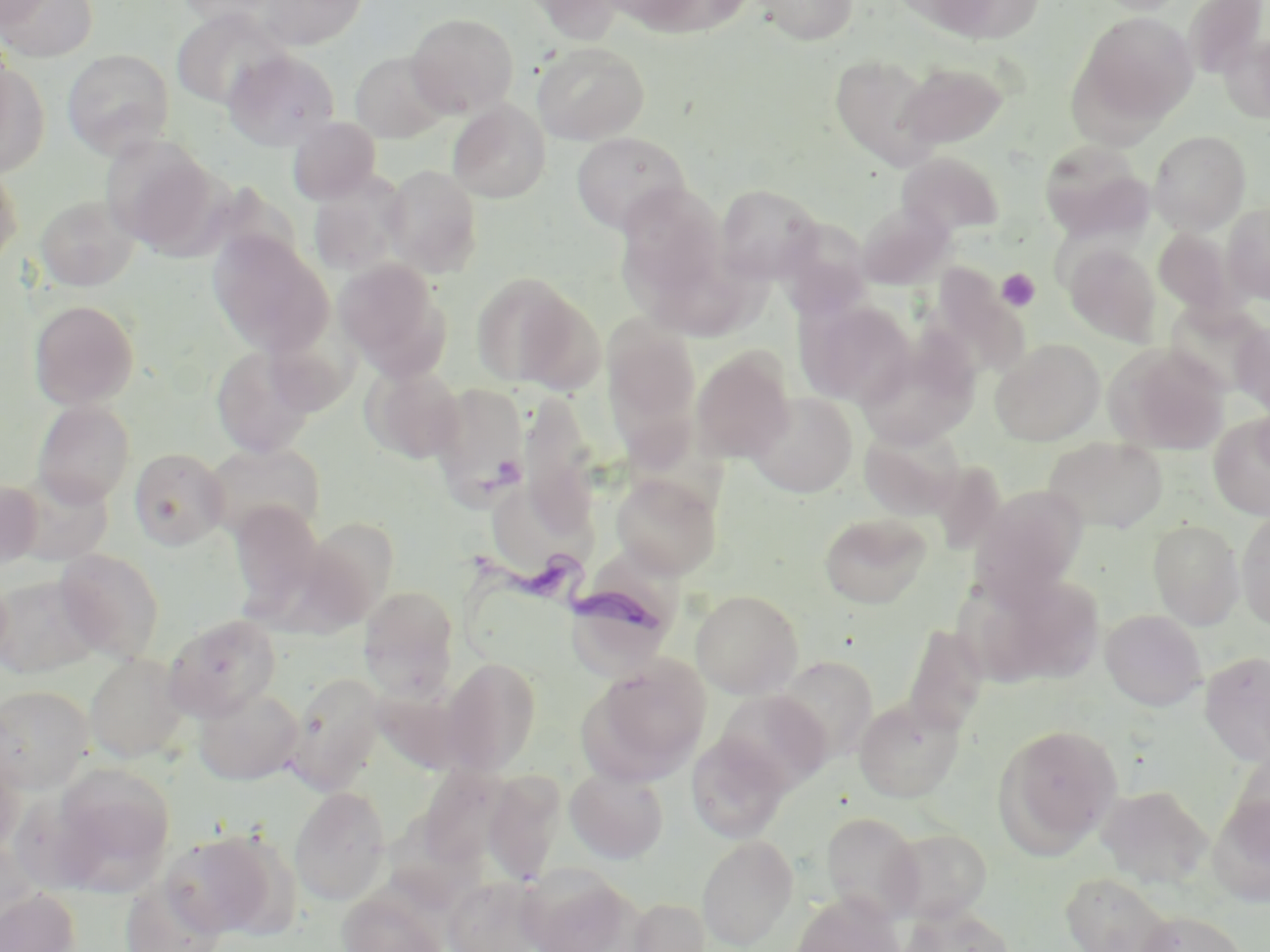

slide_level_diagnosis: Trypanosoma brucei
stain: May-Grünwald-Giemsa
platelet_locations: 'approximate bounding boxes as (x1,y1)-(x2,y2) corner pairs in pixels: (997,268)-(1040,312)'
magnification: 1000x
preparation: thin blood film
trypanosoma_brucei_locations: 'approximate bounding boxes as (x1,y1)-(x2,y2) corner pairs in pixels: (461,548)-(664,636)'
field_of_view: single
image_size: 1270×952 pixels
modality: optical microscopy
uninfected_red_blood_cell_locations: 'approximate bounding boxes as (x1,y1)-(x2,y2) corner pairs in pixels: (0,0)-(54,29), (174,0)-(287,27), (255,0)-(367,50), (522,0)-(627,43), (617,0)-(753,36), (752,0)-(859,45), (908,0)-(1046,45), (1089,0)-(1192,15), (1185,0)-(1269,79), (1,1)-(99,63), (171,8)-(288,109), (1079,11)-(1198,126), (406,12)-(519,117), (1220,32)-(1270,123), (531,41)-(649,145), (222,48)-(340,150), (62,49)-(174,158), (350,51)-(451,143), (830,54)-(942,170), (899,61)-(1010,148), (0,62)-(50,176), (447,100)-(551,203), (288,116)-(382,205), (1149,130)-(1251,233), (571,131)-(691,235), (100,135)-(222,255), (1038,139)-(1153,243), (896,151)-(1004,239), (0,164)-(23,269), (381,165)-(484,277), (308,176)-(405,278), (714,183)-(824,284), (616,184)-(729,309), (35,195)-(139,291), (855,203)-(954,290), (1222,203)-(1270,304), (770,219)-(878,322), (1154,228)-(1239,316), (207,231)-(334,358), (1064,243)-(1161,344), (333,258)-(450,378), (470,272)-(585,389), (796,297)-(915,407), (29,299)-(139,410), (1166,301)-(1268,397), (272,312)-(363,419), (1232,320)-(1270,418), (602,321)-(702,454), (856,333)-(981,449), (990,338)-(1105,445), (1104,343)-(1230,454), (210,344)-(319,458), (691,347)-(795,463), (361,363)-(464,463), (428,383)-(529,504), (520,391)-(601,533), (746,392)-(858,497), (32,400)-(136,506), (1208,414)-(1270,520), (859,425)-(963,520), (1044,437)-(1168,533), (202,442)-(326,542), (129,447)-(230,550), (9,469)-(114,565), (611,474)-(722,578), (0,481)-(43,569), (969,484)-(1088,605), (487,487)-(603,571), (228,501)-(324,617), (1236,509)-(1270,630), (820,512)-(932,608), (311,519)-(401,639), (1148,519)-(1245,629), (55,548)-(165,663), (961,570)-(1104,689), (0,571)-(12,671), (0,575)-(102,677), (358,585)-(460,697), (691,589)-(803,698), (1100,609)-(1206,711), (163,614)-(282,721), (903,623)-(990,736), (1199,651)-(1270,767), (85,654)-(190,763), (774,656)-(879,763), (441,657)-(542,775), (581,657)-(712,783), (285,671)-(387,791), (0,685)-(94,792), (193,686)-(304,785), (715,689)-(832,794), (853,697)-(964,803), (993,723)-(1123,855), (686,732)-(791,844), (1226,745)-(1270,855), (0,747)-(23,861), (51,764)-(176,894), (417,766)-(516,871), (565,766)-(669,863), (483,770)-(565,886), (1096,785)-(1212,888), (289,786)-(391,906), (1208,790)-(1270,906), (820,812)-(925,922), (886,827)-(993,923), (161,829)-(290,938), (696,834)-(799,951), (518,865)-(640,951), (1060,871)-(1178,952), (120,874)-(229,952), (443,874)-(548,952), (0,887)-(81,952), (336,888)-(450,952), (789,893)-(905,952), (624,896)-(711,952), (901,905)-(1015,952), (1133,910)-(1251,952)'